Classify this cell by malaria status.
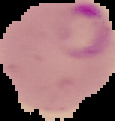
It is parasitized.

{
  "image_type": "segmented cell region on a black background",
  "image_size": "115×121 pixels",
  "preparation": "thin blood film"
}